Give the extent of all Plasmodium falciparum-infected red blood cells.
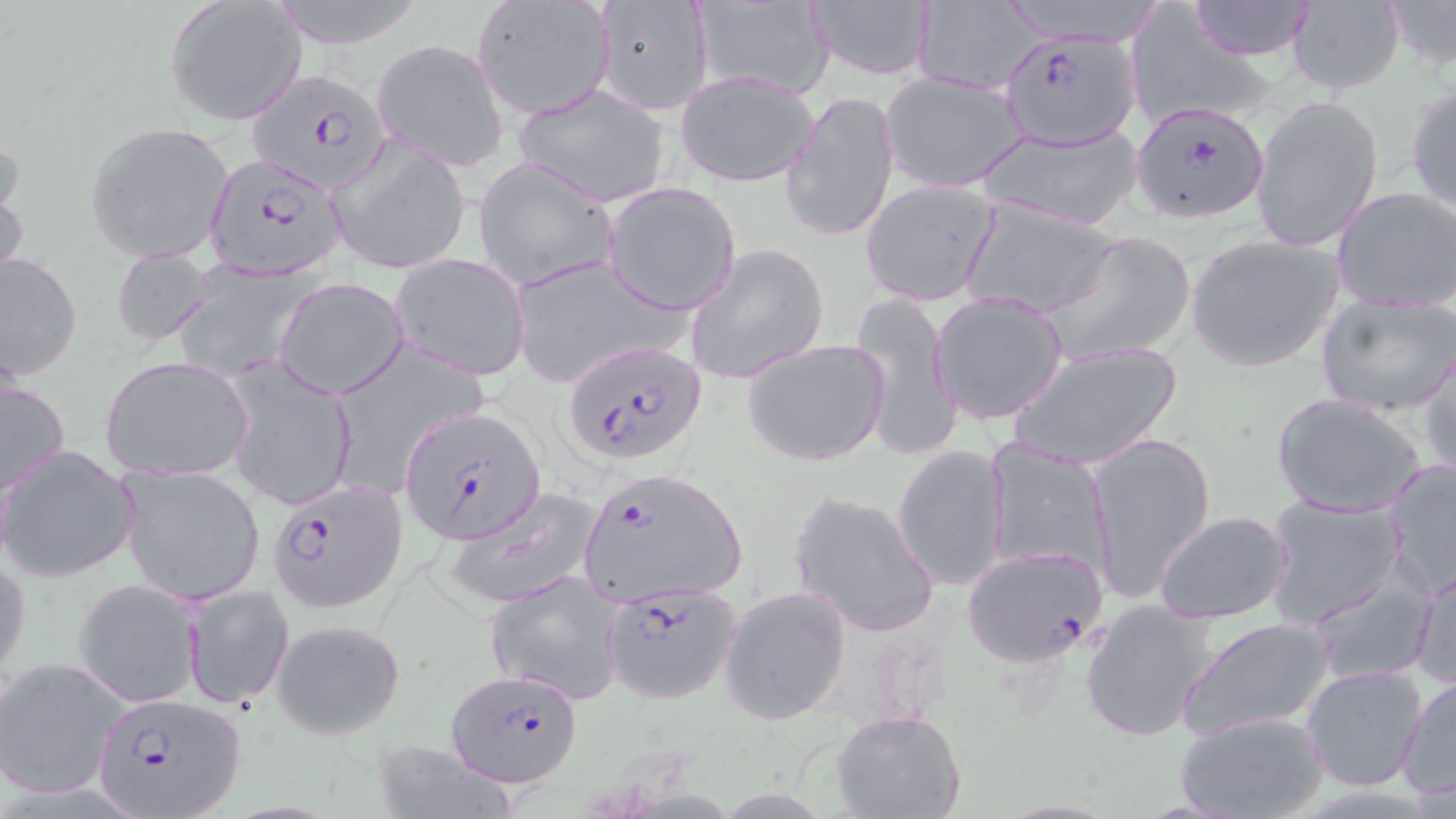

Approximate bounding boxes as (x1, y1, x2, y2) in pixels.
Plasmodium falciparum-infected red blood cells: (991, 27, 1145, 169), (245, 68, 393, 194), (1130, 100, 1271, 224), (206, 154, 346, 279), (567, 340, 708, 465), (397, 405, 547, 545), (580, 466, 745, 609), (270, 478, 408, 612), (961, 544, 1108, 667), (600, 582, 742, 704), (447, 669, 582, 787), (92, 692, 244, 818).

slide-level diagnosis = Plasmodium falciparum
image size = 1456×819 pixels
preparation = thin blood film
modality = light microscopy
magnification = 1000x
uninfected red blood cell locations = approximate bounding boxes as (x1, y1, x2, y2) in pixels: (269, 0, 427, 49), (590, 0, 716, 116), (801, 0, 937, 80), (995, 0, 1171, 49), (1187, 0, 1319, 59), (1285, 0, 1406, 95), (1384, 0, 1456, 73), (471, 1, 613, 119), (166, 2, 306, 126), (688, 2, 834, 96), (906, 3, 1046, 93), (1125, 8, 1280, 129), (371, 38, 509, 171), (675, 71, 820, 188), (880, 71, 1029, 194), (1405, 81, 1456, 217), (514, 84, 671, 207), (781, 89, 899, 245), (1250, 94, 1384, 253), (85, 121, 235, 265), (977, 122, 1144, 231), (327, 137, 471, 275), (0, 142, 28, 283), (471, 157, 622, 291), (862, 179, 1000, 306), (602, 182, 741, 315), (1332, 187, 1456, 313), (961, 198, 1120, 319), (1042, 230, 1199, 365), (1185, 233, 1344, 374), (685, 242, 830, 386), (109, 248, 216, 348), (0, 249, 83, 381), (391, 253, 532, 380), (507, 253, 688, 389), (173, 268, 312, 381), (274, 276, 409, 399), (849, 287, 962, 462), (930, 292, 1069, 424), (1316, 292, 1456, 418), (742, 338, 892, 467), (1007, 339, 1183, 471), (326, 343, 487, 496), (1418, 344, 1455, 484), (100, 356, 253, 482), (225, 361, 358, 512), (0, 371, 71, 498), (1271, 392, 1429, 518), (1084, 430, 1216, 606), (983, 439, 1113, 579), (0, 443, 139, 582), (891, 443, 1009, 593), (1382, 458, 1456, 599), (118, 463, 265, 606), (443, 487, 604, 612), (787, 489, 941, 638), (1262, 493, 1407, 628), (1153, 510, 1295, 625), (0, 551, 30, 685), (1409, 561, 1456, 693), (1307, 564, 1438, 686), (485, 571, 627, 704), (73, 579, 202, 707), (182, 583, 293, 710), (720, 585, 851, 724), (1081, 599, 1222, 742), (1178, 616, 1335, 740), (272, 617, 406, 739), (1, 656, 129, 800), (1301, 665, 1428, 793), (1397, 676, 1456, 802), (831, 710, 968, 819), (1176, 711, 1326, 819)
stain = May-Grünwald-Giemsa
field of view = one of a larger specimen